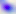
{
  "magnification": "400x",
  "identification": "Toxoplasma gondii",
  "modality": "photomicrograph"
}